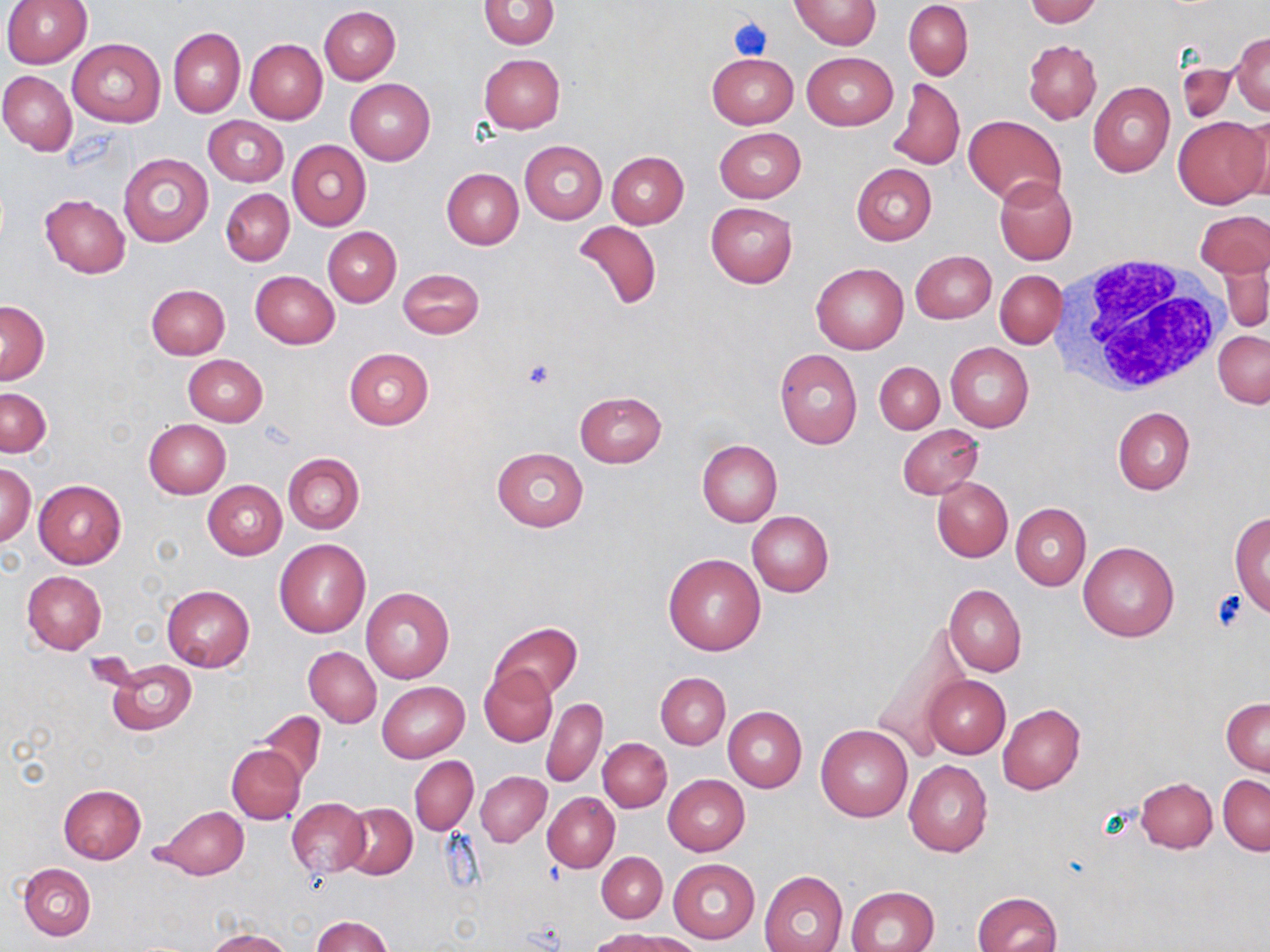

Summary:
  - Coordinate format: approximate bounding boxes as (x1,y1)-(x2,y2) corner pairs in pixels
  - Platelet locations: (729,17)-(773,60), (522,360)-(556,391), (1210,589)-(1250,630)
  - Uninfected red blood cell locations: (2,0)-(92,67), (480,0)-(558,49), (792,0)-(881,49), (1026,0)-(1101,26), (904,2)-(972,79), (319,5)-(401,84), (168,27)-(245,118), (1231,32)-(1270,115), (68,38)-(166,127), (245,39)-(327,123), (1023,40)-(1102,124), (802,51)-(898,130), (707,52)-(799,128), (479,53)-(565,133), (0,70)-(77,156), (345,78)-(436,165), (888,78)-(964,172), (1089,82)-(1175,179), (202,115)-(289,186), (963,115)-(1065,205), (1172,115)-(1270,208), (1239,116)-(1270,199), (714,127)-(805,203), (287,139)-(371,231), (519,140)-(607,223), (118,151)-(213,247), (607,151)-(688,228), (851,163)-(937,246), (441,168)-(523,250), (994,176)-(1077,265), (221,188)-(293,266), (39,193)-(131,277), (706,202)-(797,288), (1195,209)-(1270,277), (573,220)-(663,311), (322,227)-(401,307), (910,250)-(996,324), (1219,254)-(1268,333), (812,264)-(907,354), (398,267)-(484,339), (996,270)-(1066,349), (251,271)-(339,348), (147,284)-(230,359), (0,300)-(49,384), (1213,330)-(1269,408), (945,341)-(1034,432), (343,347)-(433,429), (774,349)-(863,450), (184,355)-(268,426), (875,362)-(944,434), (1,388)-(51,457), (574,391)-(667,467), (1112,406)-(1195,494), (144,419)-(230,498), (896,424)-(984,500), (697,439)-(782,525), (492,446)-(588,531), (283,453)-(364,534), (1,463)-(35,546), (932,477)-(1013,562), (34,479)-(126,568), (203,480)-(287,559), (1011,503)-(1091,590), (747,510)-(833,596), (1231,511)-(1270,619), (274,538)-(370,638), (1078,541)-(1180,642), (663,553)-(766,655), (22,571)-(107,654), (934,581)-(1020,762), (945,585)-(1026,677), (162,586)-(255,672), (361,587)-(455,684), (489,622)-(582,702), (866,622)-(970,760), (304,647)-(381,726), (102,658)-(197,736), (479,665)-(557,748), (656,672)-(730,748), (923,675)-(1010,758), (377,681)-(469,763), (1222,696)-(1270,775), (542,697)-(607,787), (997,704)-(1085,795), (723,707)-(806,793), (256,710)-(326,786), (815,723)-(913,822), (598,737)-(671,812), (227,744)-(306,824), (410,755)-(478,835), (904,759)-(993,857), (476,771)-(551,846), (663,774)-(750,856), (1218,774)-(1269,856), (1136,777)-(1218,852), (57,784)-(145,864), (543,791)-(620,872), (288,797)-(369,877), (340,803)-(416,880), (153,806)-(248,880), (597,852)-(667,922), (668,858)-(760,943), (19,862)-(97,940), (759,870)-(849,952), (848,885)-(939,952), (972,891)-(1062,952), (311,916)-(393,952), (593,928)-(695,952), (205,929)-(293,952)
  - White blood cell locations: (1054,253)-(1231,396)
  - Slide-level diagnosis: no evidence of blood parasites
  - Image size: 1270×952 pixels
  - Modality: optical microscopy
  - Stain: May-Grünwald-Giemsa
  - Magnification: 1000x
  - Preparation: thin blood film
  - Field of view: single